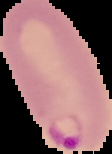
Summary:
  - Image type: cell region segmented out of the field of view; surrounding area masked to black
  - Malaria status: parasitized
  - Image size: 112×154 pixels
  - Preparation: thin blood film